Outline each Plasmodium vivax-infected red blood cell.
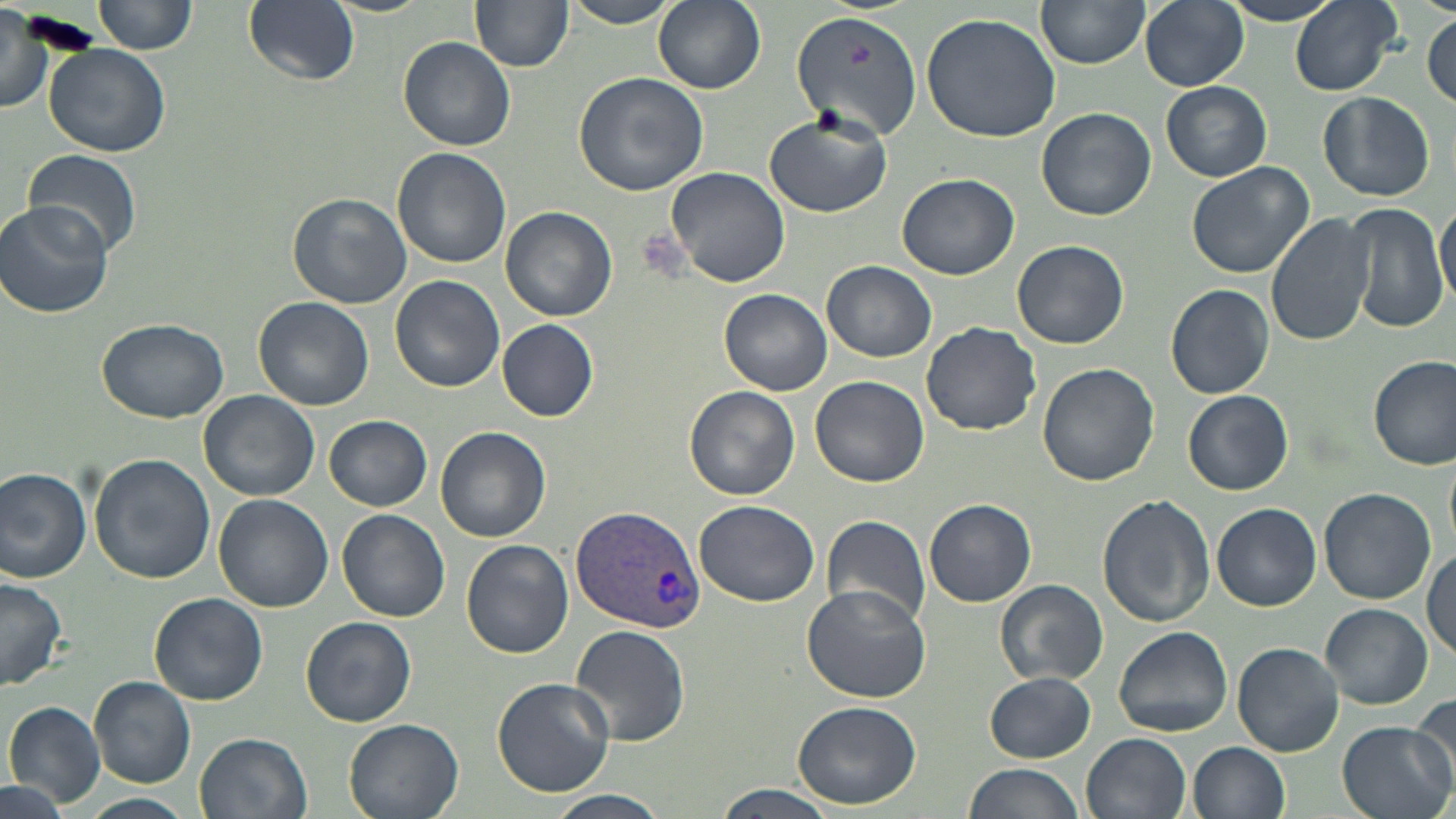

Approximate bounding boxes as named x1/y1/x2/y2 corners in pixels.
Plasmodium vivax-infected red blood cells: (x1=571, y1=503, x2=704, y2=636).

Uninfected red blood cell locations: (x1=94, y1=0, x2=197, y2=57), (x1=242, y1=0, x2=360, y2=88), (x1=319, y1=0, x2=431, y2=17), (x1=471, y1=0, x2=574, y2=71), (x1=562, y1=0, x2=682, y2=28), (x1=653, y1=0, x2=767, y2=94), (x1=1139, y1=0, x2=1248, y2=91), (x1=1289, y1=0, x2=1405, y2=97), (x1=1037, y1=1, x2=1150, y2=69), (x1=1219, y1=1, x2=1347, y2=26), (x1=0, y1=7, x2=53, y2=115), (x1=794, y1=7, x2=926, y2=140), (x1=920, y1=9, x2=1064, y2=143), (x1=1424, y1=13, x2=1455, y2=109), (x1=399, y1=36, x2=516, y2=150), (x1=41, y1=42, x2=171, y2=158), (x1=573, y1=71, x2=709, y2=196), (x1=1161, y1=81, x2=1272, y2=182), (x1=1318, y1=92, x2=1434, y2=201), (x1=1037, y1=107, x2=1156, y2=222), (x1=764, y1=110, x2=891, y2=218), (x1=21, y1=147, x2=142, y2=263), (x1=392, y1=147, x2=511, y2=269), (x1=1184, y1=161, x2=1314, y2=280), (x1=665, y1=166, x2=792, y2=289), (x1=895, y1=172, x2=1021, y2=277), (x1=287, y1=193, x2=412, y2=309), (x1=1436, y1=199, x2=1456, y2=311), (x1=1, y1=202, x2=115, y2=320), (x1=1345, y1=202, x2=1448, y2=332), (x1=501, y1=206, x2=617, y2=322), (x1=1266, y1=211, x2=1379, y2=344), (x1=1011, y1=239, x2=1130, y2=350), (x1=823, y1=261, x2=935, y2=361), (x1=391, y1=274, x2=503, y2=393), (x1=1166, y1=284, x2=1275, y2=399), (x1=719, y1=289, x2=832, y2=395), (x1=254, y1=296, x2=376, y2=410), (x1=96, y1=319, x2=229, y2=423), (x1=497, y1=320, x2=599, y2=420), (x1=921, y1=321, x2=1041, y2=435), (x1=1369, y1=354, x2=1456, y2=470), (x1=1037, y1=361, x2=1161, y2=486), (x1=810, y1=375, x2=929, y2=488), (x1=684, y1=386, x2=800, y2=501), (x1=1182, y1=389, x2=1293, y2=494), (x1=198, y1=390, x2=320, y2=502), (x1=324, y1=415, x2=433, y2=511), (x1=437, y1=427, x2=551, y2=542), (x1=89, y1=454, x2=215, y2=582), (x1=0, y1=467, x2=93, y2=583), (x1=1318, y1=487, x2=1435, y2=604), (x1=213, y1=494, x2=332, y2=612), (x1=1097, y1=495, x2=1215, y2=628), (x1=923, y1=499, x2=1037, y2=608), (x1=692, y1=500, x2=821, y2=605), (x1=1212, y1=502, x2=1321, y2=611), (x1=338, y1=508, x2=450, y2=621), (x1=822, y1=514, x2=932, y2=627), (x1=460, y1=540, x2=574, y2=659), (x1=1423, y1=549, x2=1456, y2=659), (x1=0, y1=574, x2=69, y2=693), (x1=994, y1=579, x2=1109, y2=686), (x1=801, y1=581, x2=935, y2=702), (x1=151, y1=593, x2=269, y2=706), (x1=1320, y1=603, x2=1432, y2=709), (x1=301, y1=616, x2=417, y2=727), (x1=571, y1=625, x2=692, y2=745), (x1=1114, y1=626, x2=1233, y2=737), (x1=1232, y1=643, x2=1343, y2=757), (x1=986, y1=673, x2=1095, y2=762), (x1=88, y1=676, x2=195, y2=788), (x1=490, y1=677, x2=615, y2=797), (x1=1408, y1=694, x2=1456, y2=790), (x1=794, y1=701, x2=921, y2=808), (x1=4, y1=702, x2=105, y2=808), (x1=344, y1=718, x2=464, y2=819), (x1=1334, y1=719, x2=1455, y2=819), (x1=194, y1=732, x2=314, y2=819), (x1=1082, y1=732, x2=1189, y2=819), (x1=1188, y1=741, x2=1291, y2=819), (x1=961, y1=763, x2=1087, y2=819), (x1=0, y1=779, x2=73, y2=819), (x1=711, y1=783, x2=841, y2=819), (x1=544, y1=790, x2=672, y2=819), (x1=82, y1=792, x2=194, y2=818). Slide-level diagnosis: Plasmodium vivax. Optical microscopy. Image is 1456×819 pixels. Captured at 1000x magnification. May-Grünwald-Giemsa stain. Thin blood smear. Single field of view.